Classify this cell by malaria status.
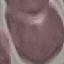

Uninfected.

Summary:
  - Image type: cell patch, automatically extracted from a larger field of view and resized to 64 × 64 pixels
  - Preparation: thin smear
  - Capture: smartphone camera at the microscope eyepiece
  - Stain: Giemsa